Classify this cell by malaria status.
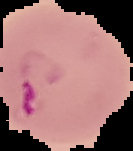

It is parasitized.

Summary:
  - Image size: 133×151 pixels
  - Preparation: thin blood smear
  - Image type: segmented cell region with the area outside set to black